Give the position of every malaria parasite.
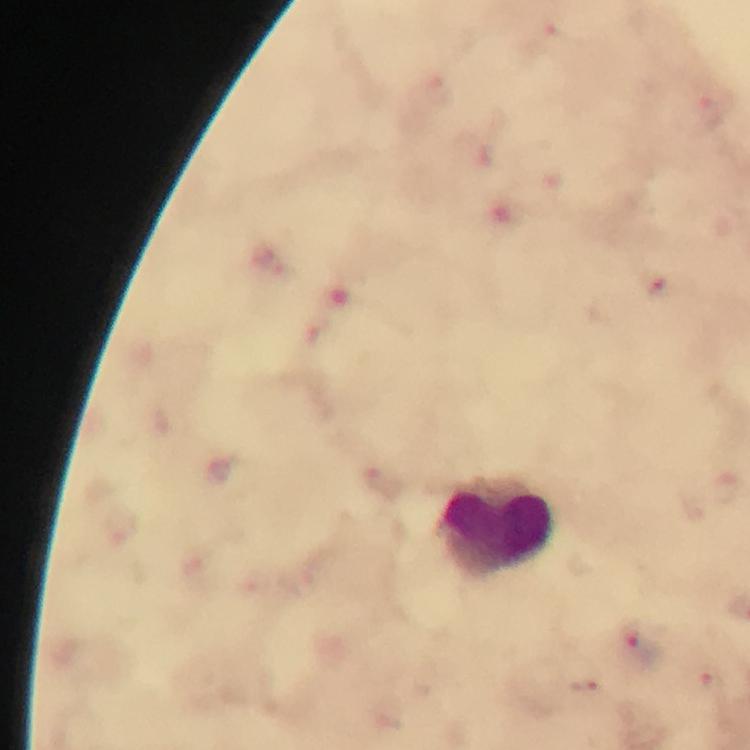

Approximate centers as [x, y] in pixels.
Malaria parasites: [386, 482], [640, 646], [712, 686], [589, 687].

Leukocyte locations: [496, 528]. 100x magnification. Immersion oil was used. Smartphone photograph taken through a microscope. Giemsa stain. Thick smear. Cropped region of a single field of view. Image is 750×750 pixels. From a malaria diagnostic workup.